State the blood parasite species.
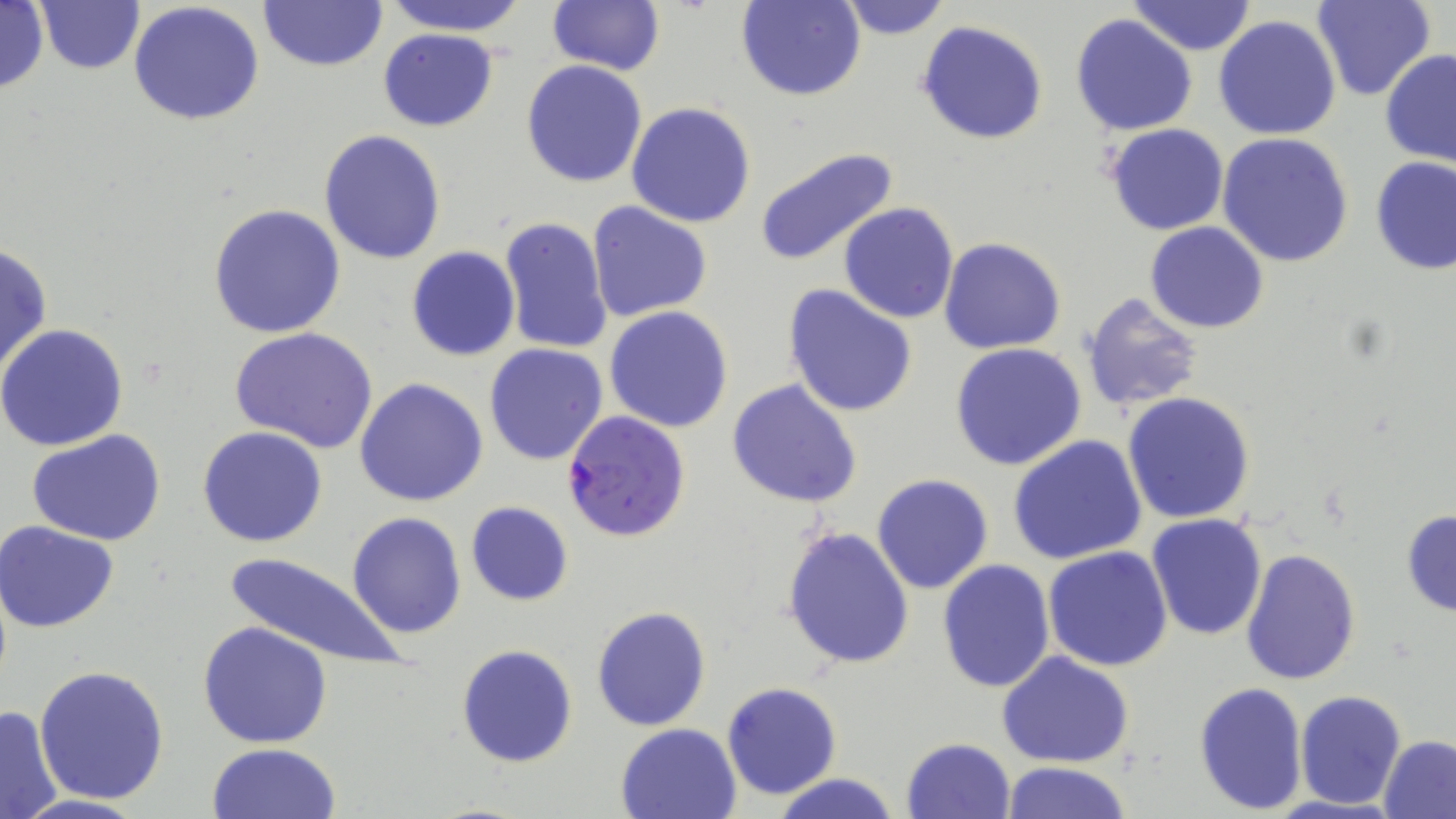

Plasmodium falciparum.

{
  "magnification": "1000x",
  "field_of_view": "one of a larger specimen",
  "modality": "light microscopy",
  "stain": "May-Grünwald-Giemsa",
  "uninfected_red_blood_cell_locations": "approximate bounding boxes as (x1,y1)-(x2,y2) corner pairs in pixels: (0,0)-(50,98), (34,0)-(144,74), (258,0)-(387,71), (380,0)-(530,34), (547,0)-(666,75), (737,0)-(865,101), (833,0)-(952,40), (1310,0)-(1437,102), (129,2)-(263,128), (1125,2)-(1258,56), (1071,13)-(1198,136), (1213,14)-(1342,141), (916,19)-(1049,145), (377,29)-(498,130), (1380,48)-(1456,166), (521,60)-(649,187), (626,102)-(757,228), (1106,124)-(1229,236), (319,129)-(448,265), (1217,132)-(1354,268), (755,147)-(899,268), (1369,157)-(1456,276), (586,201)-(713,322), (839,202)-(959,323), (208,203)-(347,340), (497,215)-(614,358), (1145,222)-(1269,333), (939,237)-(1067,354), (0,241)-(52,377), (407,246)-(520,363), (786,285)-(917,416), (1080,291)-(1205,414), (604,306)-(733,432), (0,323)-(130,450), (229,327)-(379,453), (949,342)-(1087,470), (483,343)-(610,466), (354,377)-(488,506), (727,378)-(862,507), (1122,391)-(1255,524), (198,427)-(328,549), (25,429)-(168,548), (1008,435)-(1147,565), (872,474)-(994,594), (465,502)-(574,606), (1401,507)-(1456,617), (347,512)-(466,639), (1146,515)-(1267,642), (0,521)-(122,634), (782,526)-(914,670), (1043,546)-(1174,671), (1240,548)-(1362,686), (223,549)-(407,674), (936,560)-(1055,692), (591,605)-(711,732), (198,621)-(333,750), (456,643)-(579,769), (997,652)-(1135,768), (35,665)-(169,802), (1193,681)-(1308,815), (721,682)-(844,800), (1295,690)-(1406,810), (0,704)-(65,818), (616,722)-(741,818), (1380,735)-(1456,818), (900,737)-(1017,819), (208,744)-(341,819), (1002,761)-(1132,818), (766,774)-(908,819), (5,792)-(153,819)",
  "plasmodium_falciparum_infected_red_blood_cell_locations": "approximate bounding boxes as (x1,y1)-(x2,y2) corner pairs in pixels: (561,409)-(693,543)",
  "image_size": "1456×819 pixels",
  "preparation": "thin blood film"
}